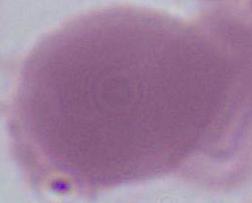
Summary:
  - Identification: erythrocyte
  - Modality: micrograph
  - Magnification: 1000x